Give the position of each Plasmodium falciparum parasite with its life-cycle stage, each leukocyte, and any debris.
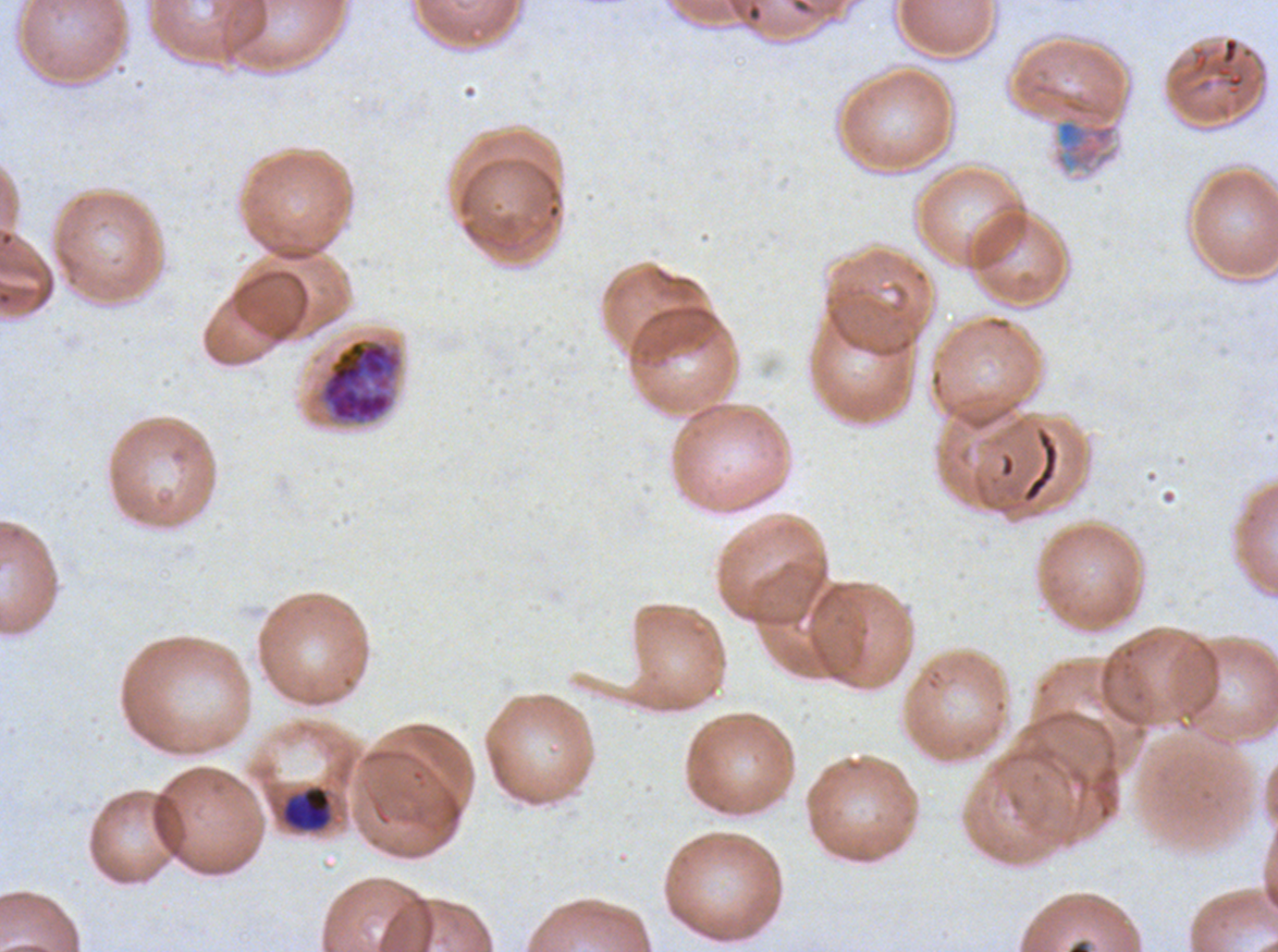

Approximate bounding boxes as (x1, y1, x2, y2) in pixels.
Mid trophozoites: (281, 785, 332, 832).
Late schizonts: (319, 337, 402, 425).
Debris: (1214, 36, 1246, 96), (1054, 119, 1117, 168), (1021, 428, 1059, 504).
No rings, late-ring/early-trophozoite forms, late trophozoites, early schizonts, segmenters, gametocytes, or leukocytes observed.

image size = 1278×952 pixels
stain = Giemsa
life-cycle stages observed = mid trophozoite, late schizont
field of view = sub-image separated from a larger composite
preparation = thin blood smear
specimen = ex-vivo Plasmodium falciparum culture from a patient in The Gambia, grown for 24 to 48 hours